Identify the blood parasite species.
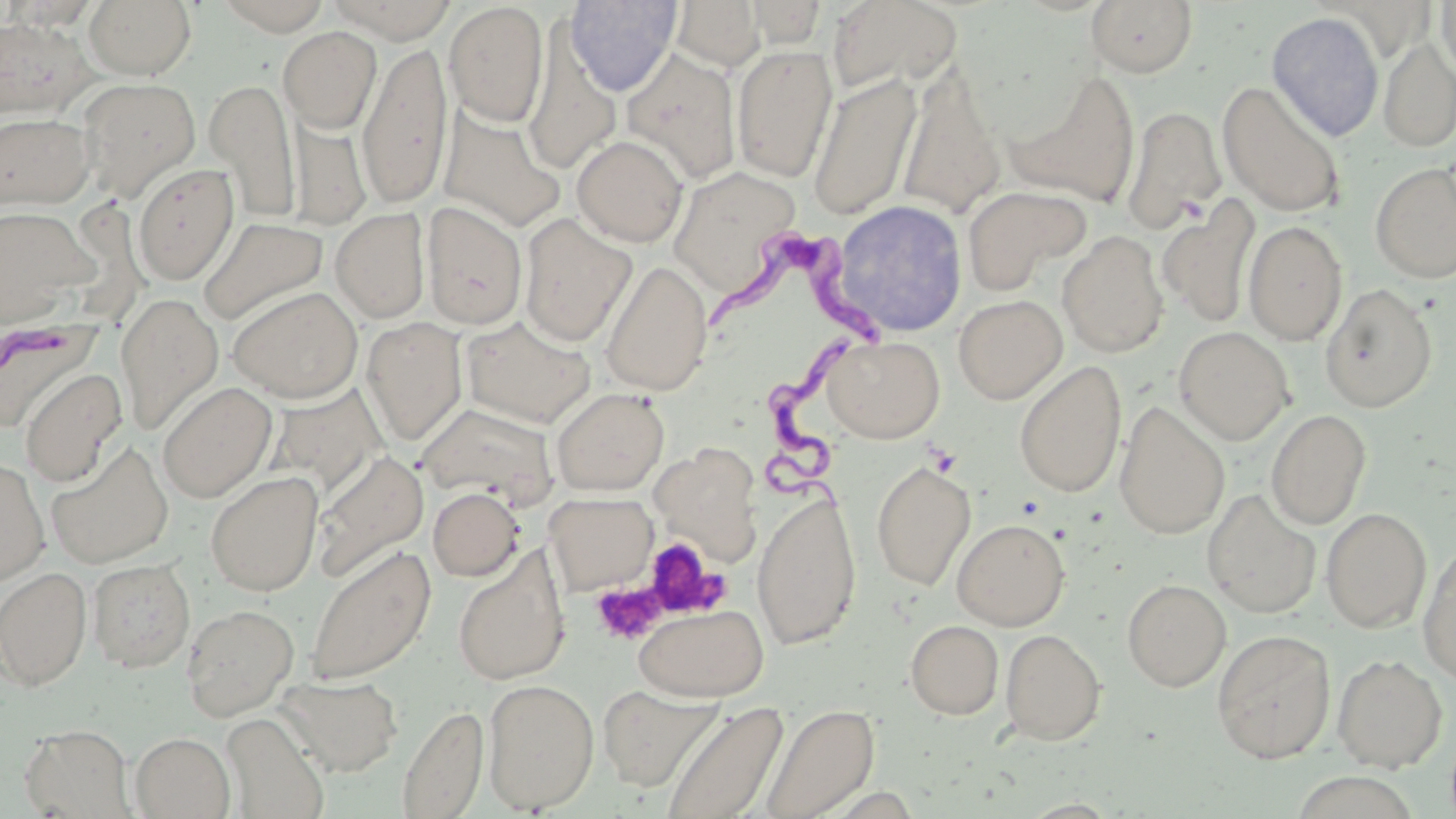

Trypanosoma brucei.

Summary:
  - Coordinate format: approximate bounding boxes as (x1, y1, x2, y2) in pixels
  - Uninfected red blood cell locations: (84, 0, 197, 81), (214, 0, 333, 35), (325, 0, 459, 42), (564, 0, 682, 97), (826, 0, 963, 97), (1087, 0, 1199, 78), (1435, 0, 1456, 82), (669, 1, 765, 71), (743, 1, 829, 48), (444, 2, 548, 127), (1266, 12, 1385, 141), (0, 16, 97, 120), (277, 27, 382, 132), (523, 27, 621, 175), (1378, 37, 1456, 153), (359, 41, 453, 211), (731, 44, 839, 183), (620, 48, 742, 185), (898, 61, 1006, 220), (1004, 71, 1142, 210), (808, 74, 922, 221), (76, 77, 201, 200), (205, 78, 301, 222), (1217, 81, 1345, 218), (1122, 105, 1226, 234), (438, 107, 566, 232), (0, 112, 95, 210), (287, 113, 370, 232), (571, 135, 688, 247), (1370, 162, 1456, 284), (133, 163, 239, 286), (668, 165, 804, 297), (962, 185, 1091, 294), (1157, 196, 1261, 328), (833, 200, 968, 337), (422, 202, 528, 330), (0, 205, 99, 328), (331, 208, 430, 324), (518, 214, 636, 347), (198, 216, 329, 326), (1243, 220, 1348, 345), (1057, 230, 1169, 358), (599, 259, 713, 396), (1320, 283, 1437, 412), (228, 286, 363, 403), (115, 293, 224, 436), (953, 294, 1067, 404), (460, 317, 596, 428), (0, 318, 98, 433), (361, 318, 468, 446), (1173, 326, 1294, 445), (822, 334, 945, 443), (1014, 360, 1127, 499), (19, 367, 127, 487), (157, 381, 277, 503), (269, 384, 389, 498), (550, 387, 669, 495), (418, 401, 559, 505), (1114, 402, 1230, 540), (1265, 409, 1371, 530), (45, 441, 173, 569), (650, 443, 764, 564), (312, 449, 429, 582), (0, 458, 50, 585), (871, 460, 976, 591), (205, 471, 324, 595), (427, 487, 525, 581), (1202, 489, 1322, 619), (544, 492, 658, 595), (752, 492, 863, 650), (1321, 507, 1432, 632), (952, 518, 1070, 630), (304, 543, 436, 686), (1418, 543, 1456, 686), (453, 545, 570, 685), (88, 559, 195, 672), (0, 567, 92, 690), (1122, 579, 1231, 691), (181, 603, 299, 721), (634, 604, 769, 701), (905, 620, 1003, 719), (1000, 629, 1106, 745), (1212, 629, 1336, 763), (1332, 654, 1448, 772), (276, 675, 404, 776), (482, 678, 600, 813), (598, 684, 723, 792), (660, 701, 788, 819), (398, 703, 488, 819), (760, 703, 879, 819), (221, 712, 329, 819), (19, 724, 135, 818), (130, 732, 235, 818)
  - Trypanosoma brucei locations: (704, 235, 898, 361), (765, 340, 867, 518)
  - Platelet locations: (641, 537, 724, 618), (590, 581, 666, 646)
  - Modality: optical microscopy
  - Image size: 1456×819 pixels
  - Stain: May-Grünwald-Giemsa
  - Field of view: single
  - Magnification: 1000x
  - Preparation: thin blood film